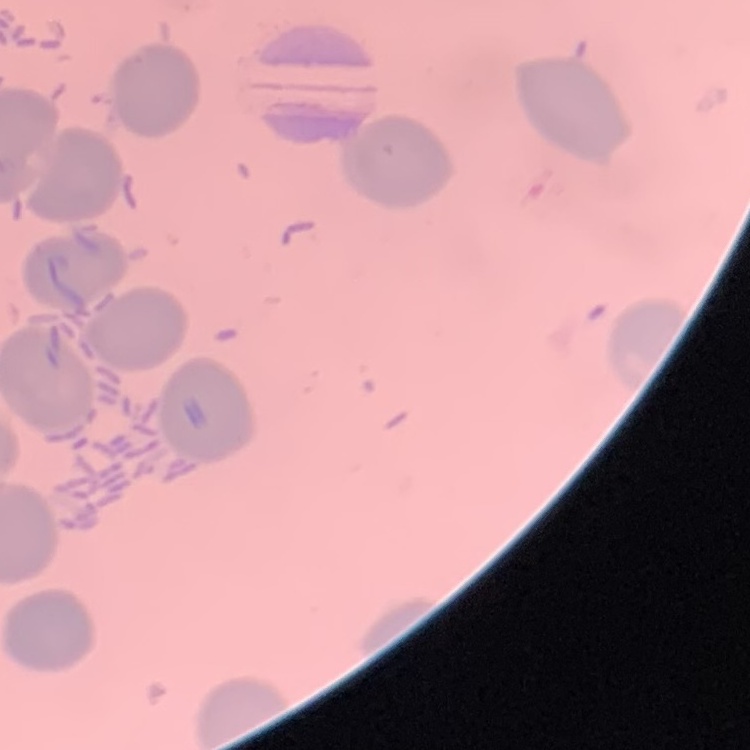

The erythrocytes exhibit no rouleaux formation. Field's or Giemsa stain. One tile cut from a larger photomicrograph. Thin blood smear.